Assess this cell for malaria.
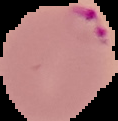

It is parasitized.

Summary:
  - Image type: segmented cell region with the area outside set to black
  - Image size: 118×121 pixels
  - Preparation: thin blood film